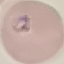
Result: malaria parasites identified. Giemsa stain. Acquired by smartphone through the microscope eyepiece. Thin blood film. Automatically extracted cell patch, resized to 64 × 64 pixels.